State the blood parasite species.
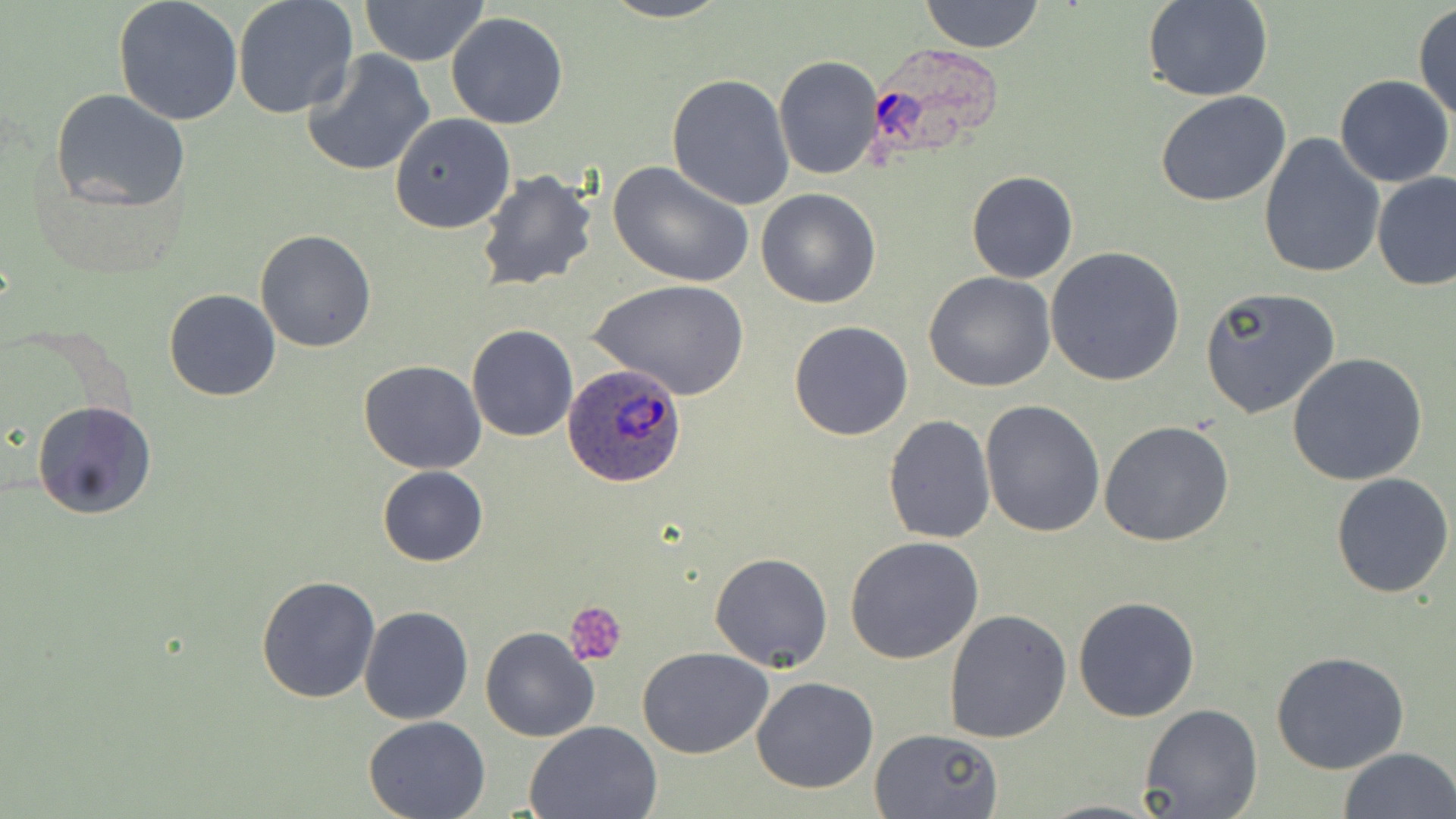

Plasmodium ovale.

Summary:
  - Coordinate format: approximate bounding boxes as (x1, y1, x2, y2) in pixels
  - Uninfected red blood cell locations: (112, 0, 243, 124), (232, 0, 358, 119), (597, 0, 734, 24), (919, 0, 1046, 52), (1143, 0, 1274, 103), (358, 1, 490, 65), (1412, 4, 1456, 122), (445, 12, 568, 129), (302, 48, 437, 178), (774, 55, 882, 180), (666, 74, 796, 210), (1333, 75, 1454, 188), (50, 88, 189, 210), (1155, 92, 1293, 207), (390, 113, 516, 234), (1258, 133, 1385, 279), (607, 160, 754, 288), (476, 169, 599, 292), (966, 171, 1078, 283), (1372, 172, 1455, 293), (757, 188, 880, 309), (254, 229, 377, 352), (1044, 247, 1186, 386), (923, 272, 1056, 392), (588, 279, 749, 400), (1199, 287, 1341, 419), (164, 288, 280, 401), (788, 320, 913, 439), (467, 325, 578, 441), (1287, 352, 1427, 486), (358, 360, 486, 474), (980, 400, 1106, 539), (32, 401, 158, 521), (883, 414, 995, 542), (1100, 419, 1234, 546), (377, 466, 488, 566), (1332, 472, 1454, 596), (844, 535, 987, 664), (710, 552, 833, 672), (256, 574, 383, 704), (1072, 595, 1201, 722), (359, 605, 473, 724), (945, 610, 1071, 742), (480, 627, 600, 743), (637, 647, 773, 759), (1269, 651, 1411, 775), (749, 676, 879, 793), (1137, 703, 1264, 819), (363, 716, 491, 819), (524, 720, 665, 818), (870, 726, 1002, 817), (1338, 746, 1455, 819)
  - Platelet locations: (565, 600, 627, 665)
  - Plasmodium ovale-infected red blood cell locations: (859, 48, 1017, 163), (563, 364, 691, 488)
  - Magnification: 1000x
  - Stain: May-Grünwald-Giemsa
  - Preparation: thin blood smear
  - Image size: 1456×819 pixels
  - Field of view: single
  - Modality: light microscopy